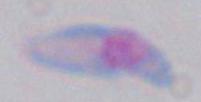
{
  "identification": "Toxoplasma gondii",
  "magnification": "1000x",
  "modality": "photomicrograph"
}